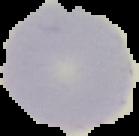
Image is 139×136 pixels. From a thin blood film. Malaria status: uninfected. Segmented cell region on a black background.